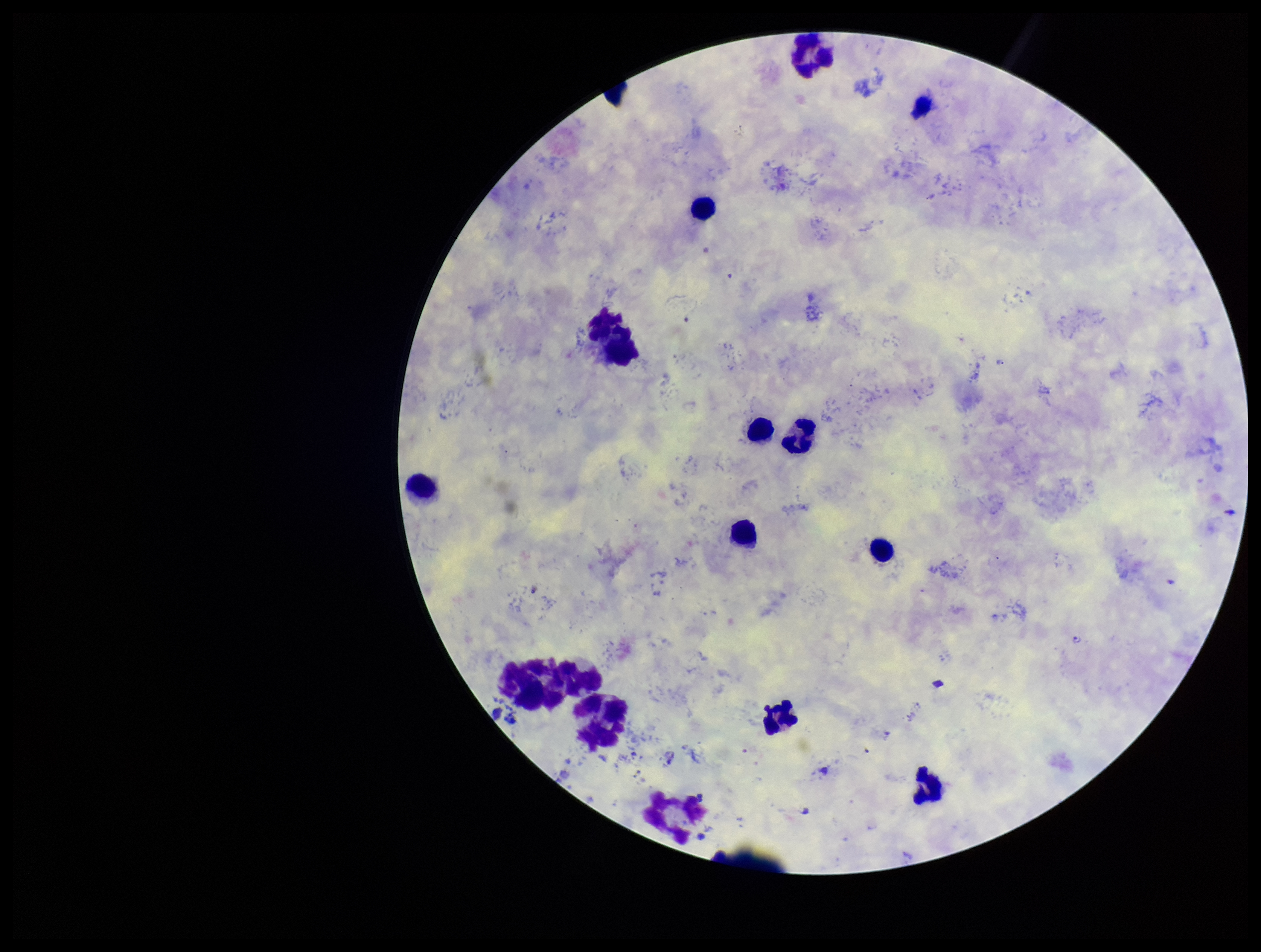

Patient malaria status: positive. Leukocyte count: 15. Parasite count: 3. Smartphone photograph taken through the eyepiece of a microscope. Preparation: thick blood smear. One field from this slide. Plasmodium parasites: seen. Species reported for this patient: Plasmodium vivax. Image is 1261×952 pixels. Stained with Giemsa.